Report the malaria status of this cell.
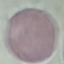

Uninfected.

Giemsa-stained preparation. Thin blood smear. Photographed with a smartphone camera at the microscope eyepiece. Automatically extracted cell patch, resized to 64 × 64 pixels.